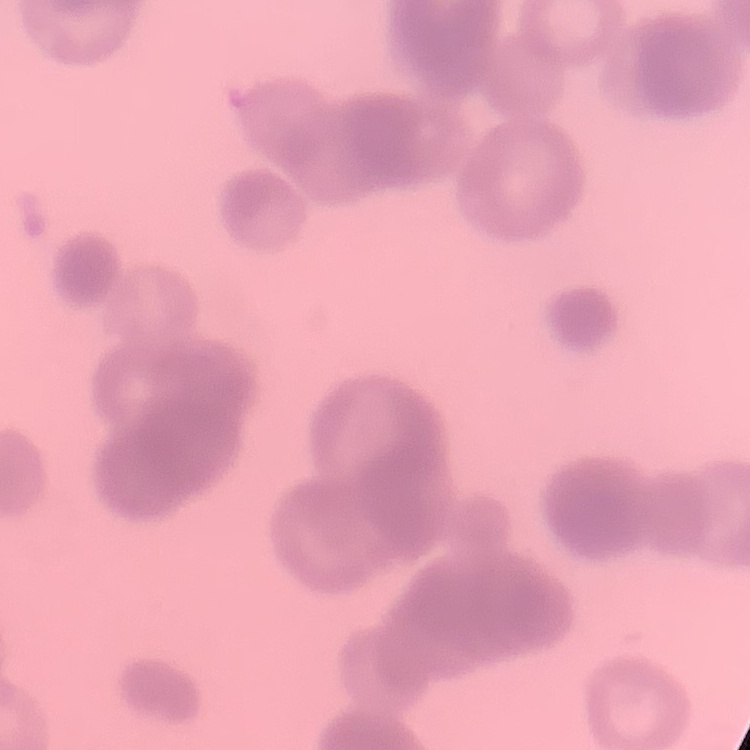

Summary:
  - Red blood cell morphology: rouleaux formation
  - Preparation: thin peripheral smear
  - Image type: square crop of a larger photomicrograph
  - Stain: Field's or Giemsa